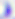 Toxoplasma gondii is seen. 400x magnification. Micrograph.